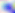 Toxoplasma gondii is shown. Micrograph. Captured at 400x magnification.